Describe the morphology of the red blood cells.
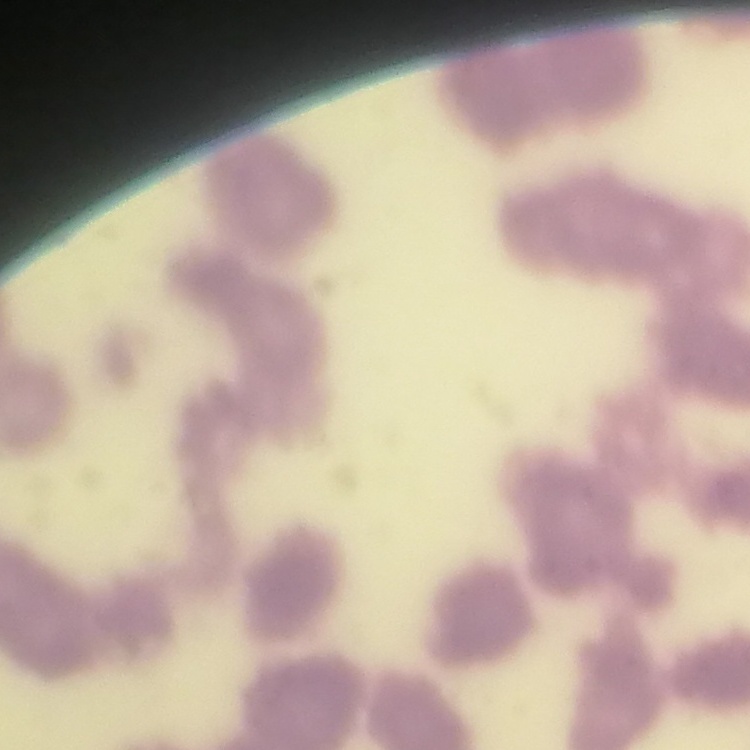

They show rouleaux formation.

Summary:
  - Preparation: thin peripheral smear
  - Stain: Field's or Giemsa
  - Image type: square crop of a larger photomicrograph